Comment on the morphology of the red blood cells.
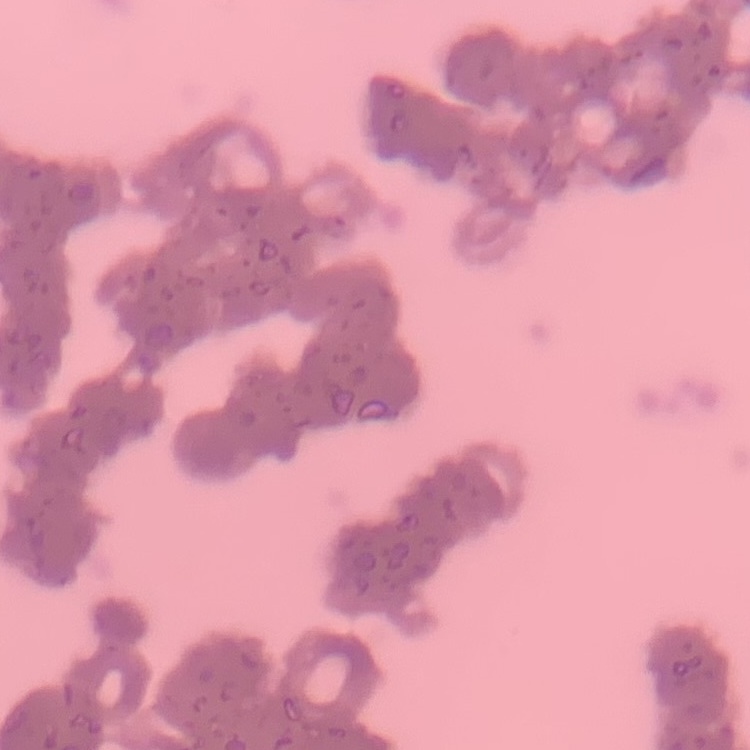

Rouleaux formation.

stain = Field's or Giemsa
preparation = thin peripheral smear
image type = square crop of a larger photomicrograph